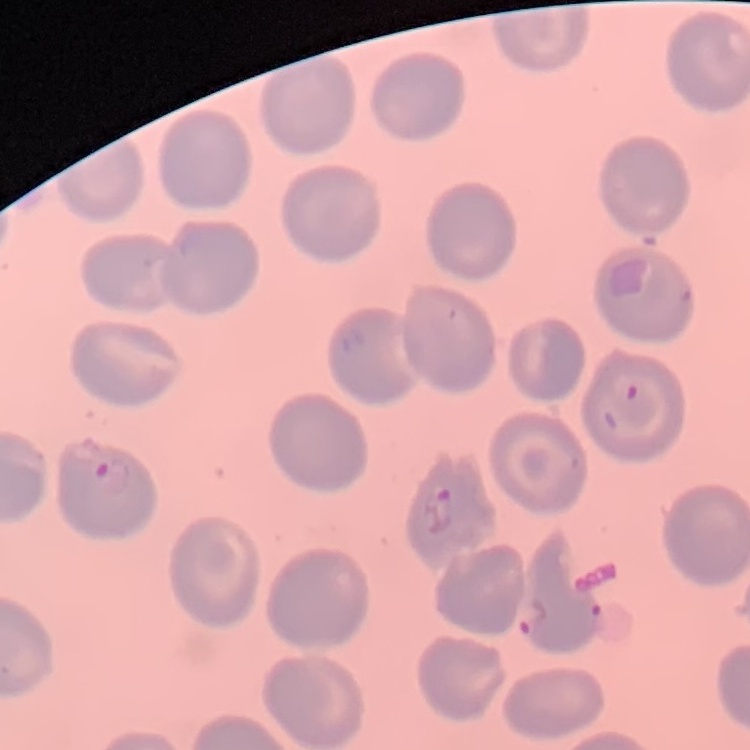 The red blood cells exhibit no rouleaux formation. One tile cut from a larger photomicrograph. Thin blood smear. Field's or Giemsa stain.